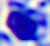

Summary:
  - Modality: micrograph
  - Magnification: 400x
  - Identification: leukocyte